Evaluate for Plasmodium parasites.
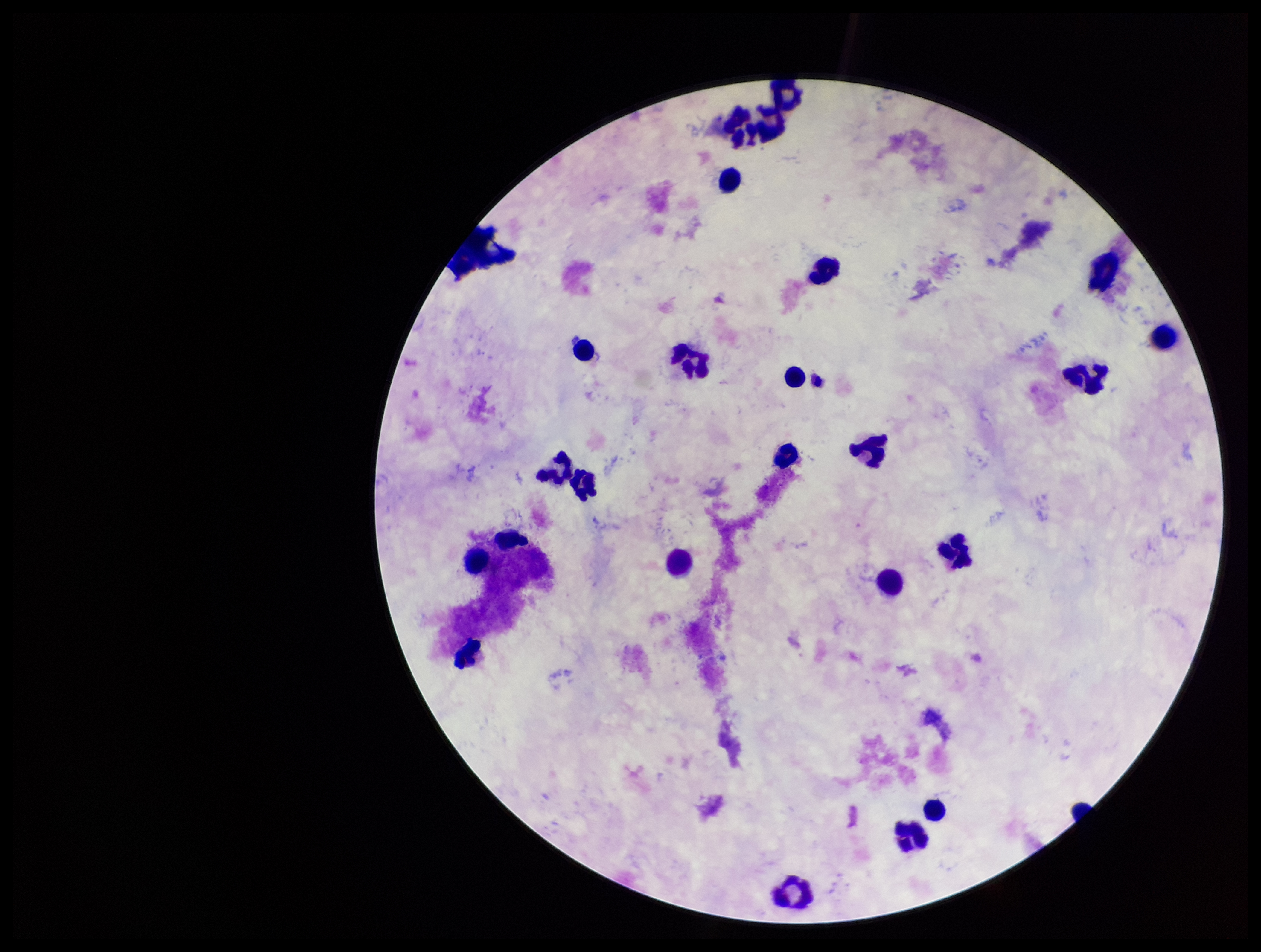
None seen.

Smartphone photograph taken through the eyepiece of a microscope. Giemsa stain. Single field of view. Leukocyte count: 24. Patient malaria status: negative. Preparation: thick blood smear. Parasite count: 0. Image is 1261×952 pixels.